Give the location of every white blood cell.
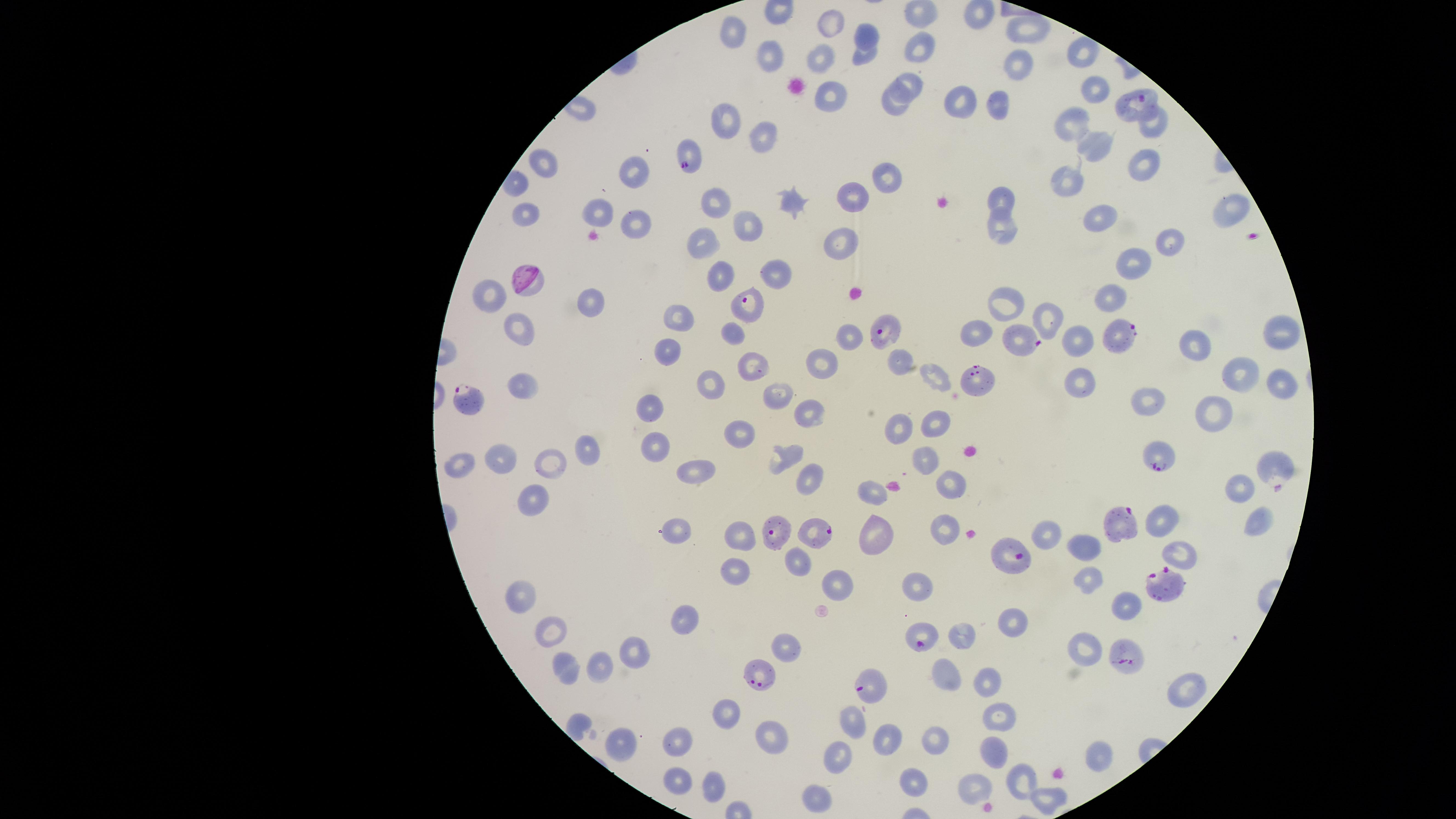

No white blood cells identified.

Approximate marker points as (x, y) in pixels.
Summary:
  - Parasitized red blood cells: (1135, 101), (686, 154), (749, 307), (885, 330), (1117, 334), (1026, 342), (976, 382), (471, 404), (1158, 458), (1271, 470), (1117, 521), (780, 527), (822, 532), (1009, 554), (1170, 584), (920, 636), (1125, 654), (758, 678), (874, 688)
  - Uninfected red blood cells: (922, 16), (832, 24), (1027, 28), (734, 29), (866, 31), (920, 49), (1081, 52), (861, 56), (765, 57), (816, 63), (1015, 69), (909, 81), (1094, 91), (828, 94), (958, 102), (997, 104), (890, 107), (724, 115), (1073, 124), (1154, 124), (761, 135), (1093, 146), (544, 165), (1136, 165), (630, 168), (883, 177), (1067, 181), (713, 198), (847, 198), (1001, 199), (791, 204), (1229, 208), (601, 210), (522, 215), (1096, 217), (745, 227), (630, 228), (996, 228), (700, 238), (840, 244), (1167, 244), (1131, 261), (774, 272), (721, 275), (1106, 297), (495, 298), (592, 305), (1006, 307), (676, 316), (1043, 316), (519, 330), (1275, 331), (730, 332), (978, 332), (847, 335), (1077, 340), (1197, 343), (669, 345), (821, 361), (898, 362), (749, 365), (1229, 369), (1279, 378), (1080, 382), (710, 383), (930, 383), (524, 385), (776, 393), (1147, 401), (646, 407), (1214, 414), (807, 415), (932, 422), (896, 429), (736, 433), (585, 443), (653, 448), (783, 456), (502, 458), (926, 458), (550, 461), (459, 465), (697, 471), (810, 479), (1239, 485), (871, 486), (952, 486), (535, 496), (1167, 517), (1256, 522), (944, 526), (1041, 529), (675, 530), (739, 535), (878, 539), (1084, 544), (1182, 557), (796, 558), (735, 573), (1087, 578), (835, 585), (918, 588), (520, 592), (1125, 606), (681, 619), (1012, 620), (550, 628), (962, 635), (1084, 648), (633, 652), (603, 665), (564, 669), (942, 677), (988, 682), (1181, 686), (723, 711), (994, 715), (854, 718), (764, 736), (882, 736), (930, 739), (675, 744), (616, 745), (994, 748), (1098, 752), (836, 756), (1026, 778), (911, 780), (670, 783), (711, 784), (978, 784), (816, 794), (1048, 801)
  - Species: Plasmodium falciparum
  - Field of view: single
  - Presence: malaria parasites seen
  - Preparation: thin smear of blood
  - Visible region: circular
  - Image size: 1456×819 pixels
  - Stain: Giemsa
  - Capture: smartphone photograph through the microscope eyepiece